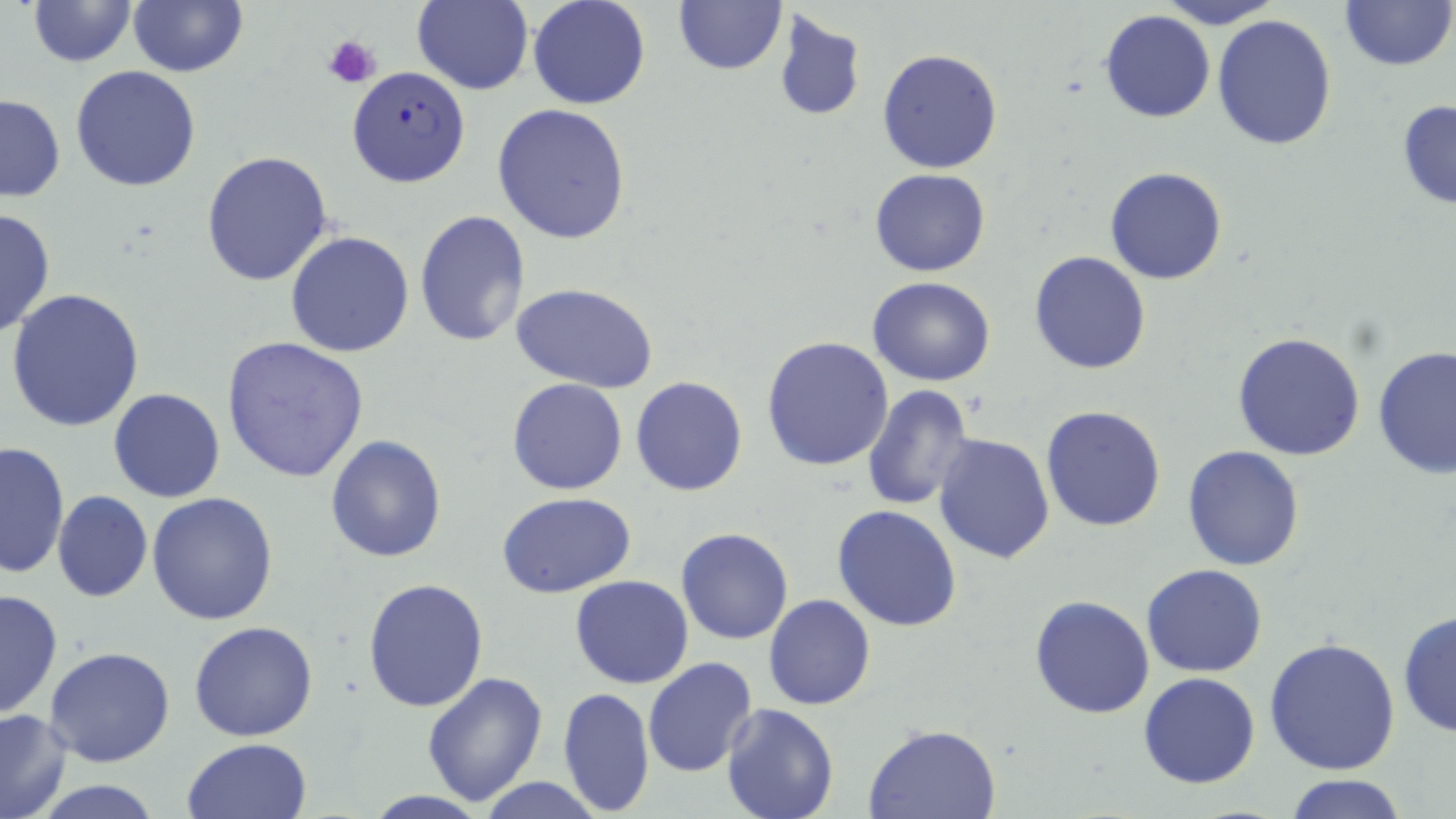
Summary:
  - Coordinate format: approximate bounding boxes as named x1/y1/x2/y2 corners in pixels
  - Platelet locations: (x1=323, y1=33, x2=382, y2=88)
  - Uninfected red blood cell locations: (x1=24, y1=0, x2=140, y2=68), (x1=528, y1=0, x2=651, y2=110), (x1=671, y1=0, x2=788, y2=76), (x1=1159, y1=0, x2=1281, y2=28), (x1=1336, y1=0, x2=1455, y2=74), (x1=411, y1=1, x2=533, y2=94), (x1=128, y1=2, x2=248, y2=77), (x1=771, y1=9, x2=866, y2=123), (x1=1100, y1=10, x2=1217, y2=124), (x1=1212, y1=13, x2=1338, y2=150), (x1=876, y1=48, x2=1004, y2=175), (x1=70, y1=65, x2=201, y2=192), (x1=1, y1=92, x2=66, y2=201), (x1=1395, y1=99, x2=1456, y2=212), (x1=491, y1=103, x2=632, y2=245), (x1=202, y1=150, x2=334, y2=287), (x1=1103, y1=165, x2=1227, y2=286), (x1=869, y1=167, x2=993, y2=277), (x1=0, y1=207, x2=56, y2=338), (x1=413, y1=209, x2=530, y2=347), (x1=286, y1=230, x2=416, y2=358), (x1=1028, y1=250, x2=1151, y2=375), (x1=868, y1=275, x2=997, y2=386), (x1=511, y1=280, x2=659, y2=393), (x1=7, y1=290, x2=148, y2=433), (x1=1231, y1=332, x2=1366, y2=461), (x1=761, y1=335, x2=896, y2=471), (x1=220, y1=337, x2=372, y2=484), (x1=1374, y1=347, x2=1456, y2=481), (x1=630, y1=376, x2=747, y2=497), (x1=506, y1=377, x2=629, y2=495), (x1=861, y1=383, x2=975, y2=511), (x1=107, y1=388, x2=225, y2=503), (x1=1041, y1=406, x2=1167, y2=532), (x1=933, y1=431, x2=1056, y2=563), (x1=325, y1=435, x2=447, y2=562), (x1=1, y1=441, x2=70, y2=580), (x1=1182, y1=444, x2=1305, y2=571), (x1=52, y1=490, x2=152, y2=603), (x1=147, y1=493, x2=278, y2=627), (x1=498, y1=493, x2=637, y2=600), (x1=832, y1=504, x2=963, y2=632), (x1=677, y1=528, x2=794, y2=645), (x1=1141, y1=564, x2=1269, y2=678), (x1=570, y1=575, x2=694, y2=689), (x1=362, y1=576, x2=489, y2=713), (x1=0, y1=589, x2=61, y2=721), (x1=763, y1=594, x2=876, y2=710), (x1=1028, y1=594, x2=1155, y2=719), (x1=1399, y1=608, x2=1456, y2=742), (x1=188, y1=620, x2=319, y2=740), (x1=1265, y1=636, x2=1402, y2=777), (x1=44, y1=646, x2=177, y2=768), (x1=643, y1=657, x2=759, y2=776), (x1=421, y1=673, x2=549, y2=807), (x1=1137, y1=673, x2=1260, y2=790), (x1=558, y1=688, x2=656, y2=814), (x1=720, y1=703, x2=838, y2=819), (x1=0, y1=707, x2=72, y2=819), (x1=863, y1=723, x2=1001, y2=818), (x1=181, y1=738, x2=313, y2=819), (x1=1282, y1=775, x2=1410, y2=818), (x1=477, y1=777, x2=600, y2=818), (x1=27, y1=779, x2=171, y2=818), (x1=362, y1=791, x2=494, y2=819)
  - Plasmodium falciparum-infected red blood cell locations: (x1=344, y1=66, x2=471, y2=189)
  - Slide-level diagnosis: Plasmodium falciparum
  - Stain: May-Grünwald-Giemsa
  - Image size: 1456×819 pixels
  - Field of view: single
  - Modality: light microscopy
  - Preparation: thin blood smear
  - Magnification: 1000x